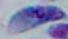
Captured at 1000x magnification. Photomicrograph. Toxoplasma gondii is shown.